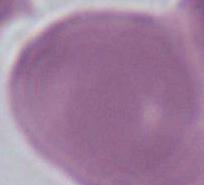
An erythrocyte is seen. Captured at 1000x magnification. Photomicrograph.